Locate every Plasmodium parasite and every leukocyte.
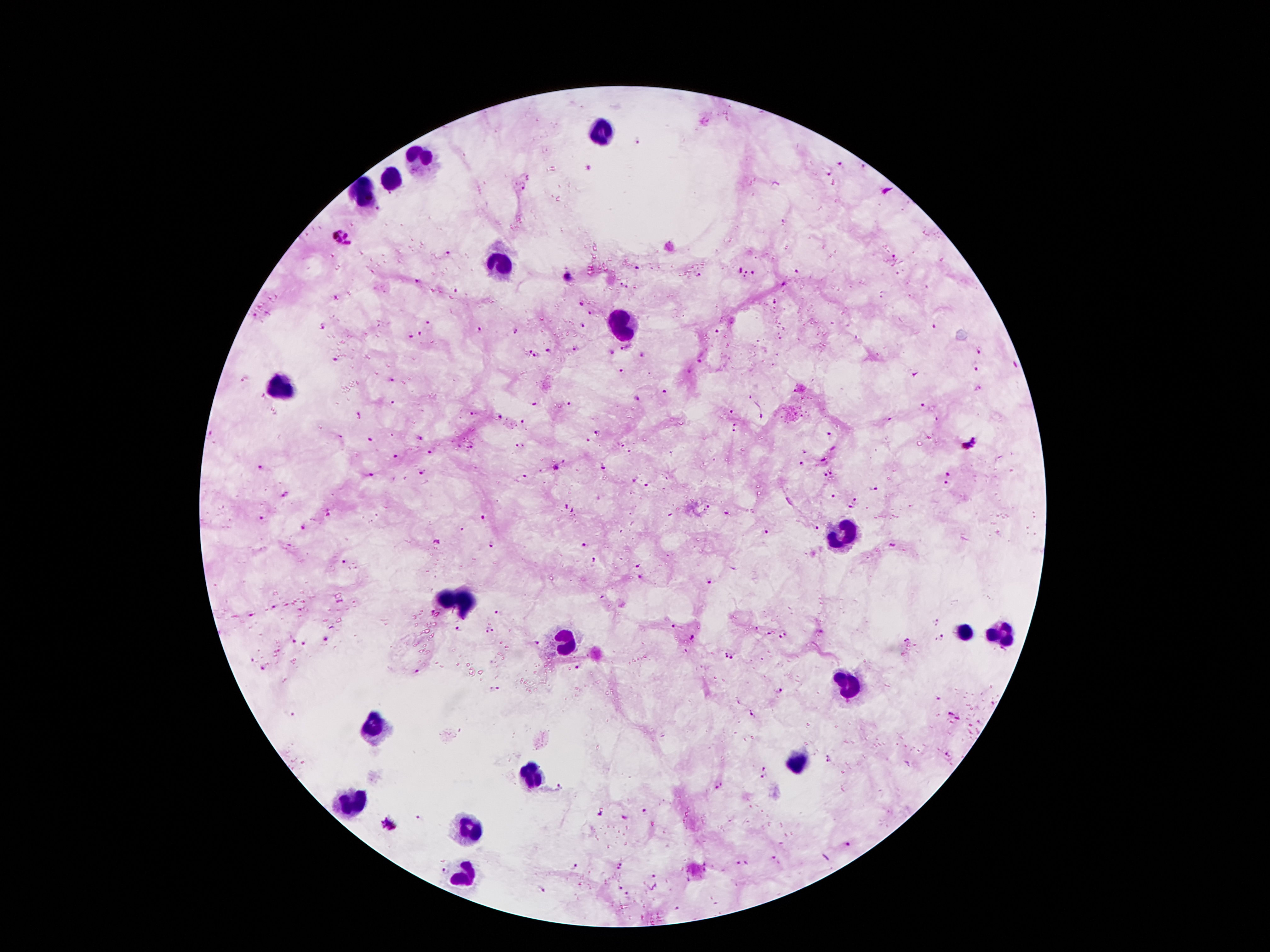

Approximate centers as {x, y} in pixels.
Plasmodium parasites: {637, 139}, {841, 163}, {863, 167}, {587, 168}, {829, 173}, {522, 186}, {785, 221}, {341, 238}, {448, 254}, {895, 256}, {637, 268}, {741, 269}, {797, 272}, {746, 274}, {753, 274}, {699, 275}, {568, 277}, {417, 280}, {622, 285}, {784, 285}, {455, 291}, {337, 297}, {581, 303}, {591, 312}, {255, 316}, {429, 321}, {323, 325}, {583, 325}, {935, 326}, {481, 328}, {516, 330}, {717, 332}, {420, 334}, {411, 338}, {625, 347}, {576, 349}, {549, 351}, {979, 351}, {528, 352}, {612, 352}, {537, 355}, {641, 357}, {335, 360}, {699, 361}, {976, 368}, {621, 371}, {391, 379}, {245, 380}, {977, 389}, {665, 392}, {637, 398}, {393, 401}, {535, 404}, {570, 404}, {923, 405}, {472, 411}, {731, 411}, {500, 415}, {360, 416}, {761, 417}, {936, 419}, {522, 421}, {735, 428}, {598, 431}, {830, 436}, {340, 437}, {418, 439}, {369, 440}, {587, 440}, {969, 442}, {520, 446}, {621, 446}, {472, 448}, {833, 449}, {805, 451}, {429, 452}, {631, 452}, {395, 456}, {824, 459}, {803, 463}, {260, 467}, {603, 467}, {557, 468}, {422, 472}, {831, 472}, {948, 473}, {370, 474}, {824, 475}, {525, 477}, {634, 478}, {945, 484}, {645, 485}, {874, 488}, {286, 494}, {833, 497}, {854, 500}, {708, 507}, {569, 509}, {849, 509}, {329, 513}, {727, 513}, {483, 517}, {304, 525}, {816, 527}, {764, 532}, {437, 542}, {583, 544}, {490, 546}, {594, 560}, {343, 561}, {637, 566}, {640, 577}, {710, 581}, {275, 607}, {433, 612}, {253, 614}, {498, 615}, {937, 622}, {673, 625}, {756, 628}, {460, 630}, {491, 631}, {768, 634}, {783, 636}, {940, 637}, {694, 638}, {326, 639}, {293, 640}, {907, 641}, {302, 643}, {536, 643}, {686, 651}, {730, 654}, {263, 668}, {576, 668}, {416, 671}, {496, 689}, {779, 691}, {949, 712}, {291, 713}, {751, 715}, {958, 718}, {948, 755}, {830, 759}, {763, 769}, {763, 778}, {719, 786}, {559, 787}, {645, 812}, {600, 815}, {419, 816}, {388, 824}, {848, 843}, {774, 858}, {737, 863}, {746, 863}, {620, 866}, {575, 867}, {445, 871}, {653, 876}, {542, 889}, {621, 889}, {627, 895}, {678, 908}.
Leukocytes: {600, 134}, {416, 163}, {395, 179}, {365, 193}, {495, 263}, {619, 322}, {279, 386}, {842, 534}, {458, 599}, {964, 634}, {999, 634}, {565, 641}, {848, 687}, {376, 725}, {798, 765}, {529, 773}, {350, 804}, {470, 830}, {464, 876}.

stain = Giemsa
preparation = thick blood smear
image size = 1270×952 pixels
capture = smartphone camera through the microscope eyepiece
magnification = 100x
patient malaria status = infected with Plasmodium falciparum
field of view = one from this slide